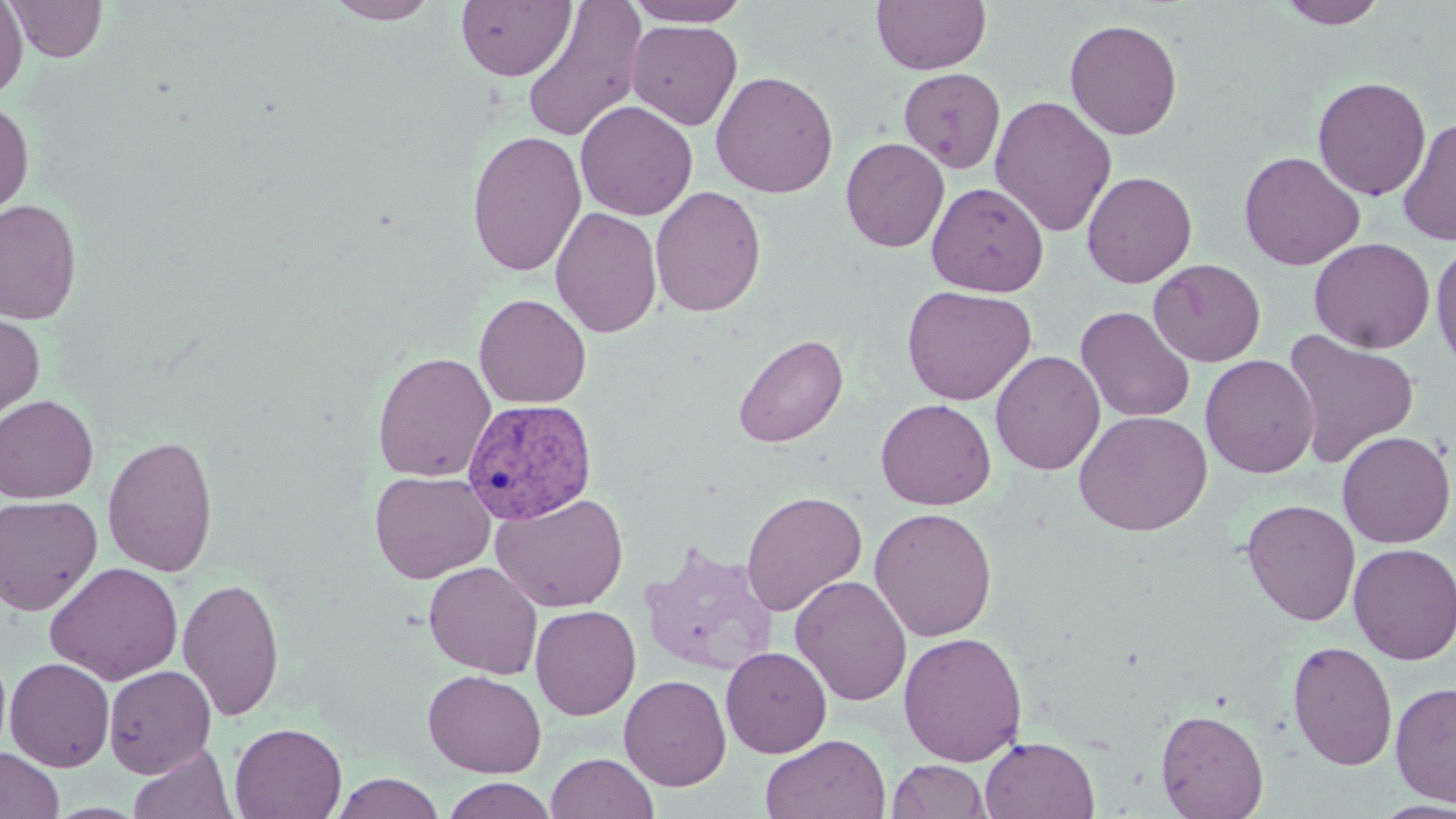

slide-level diagnosis = Plasmodium vivax
magnification = 1000x
preparation = thin blood film
stain = May-Grünwald-Giemsa
image size = 1456×819 pixels
modality = light microscopy
Plasmodium vivax-infected red blood cell locations = approximate bounding boxes as [x1, y1, x2, y2] in pixels: [461, 398, 597, 524]
uninfected red blood cell locations = approximate bounding boxes as [x1, y1, x2, y2] in pixels: [0, 0, 28, 100], [8, 0, 106, 63], [325, 0, 441, 24], [455, 0, 575, 81], [521, 0, 647, 144], [625, 0, 751, 27], [871, 0, 991, 74], [1276, 0, 1388, 29], [627, 19, 743, 130], [1064, 19, 1183, 140], [898, 67, 1006, 174], [711, 70, 839, 198], [1312, 76, 1431, 201], [990, 95, 1117, 237], [0, 100, 34, 218], [575, 100, 697, 221], [1397, 117, 1456, 247], [467, 130, 587, 277], [840, 136, 950, 253], [1239, 151, 1365, 270], [1082, 170, 1198, 288], [927, 181, 1049, 297], [650, 185, 766, 317], [0, 198, 82, 325], [550, 206, 662, 338], [1309, 237, 1435, 354], [1431, 240, 1456, 375], [1148, 259, 1266, 366], [901, 284, 1038, 406], [474, 293, 591, 409], [1076, 305, 1196, 422], [0, 311, 45, 428], [1282, 329, 1420, 468], [732, 333, 849, 448], [990, 350, 1105, 475], [372, 351, 496, 483], [1200, 354, 1320, 478], [0, 394, 99, 502], [876, 398, 996, 510], [1074, 410, 1213, 536], [1337, 430, 1455, 548], [102, 434, 219, 578], [370, 470, 495, 583], [741, 490, 867, 617], [491, 492, 628, 612], [0, 495, 103, 615], [1241, 499, 1361, 627], [869, 506, 998, 642], [639, 542, 780, 677], [1349, 542, 1456, 665], [424, 561, 543, 679], [45, 562, 183, 684], [790, 575, 912, 706], [177, 576, 286, 722], [530, 605, 641, 720], [898, 631, 1027, 766], [1287, 639, 1398, 771], [721, 646, 832, 757], [0, 647, 12, 761], [4, 657, 115, 772], [103, 664, 217, 778], [423, 669, 547, 778], [619, 674, 731, 792], [1390, 680, 1456, 808], [1156, 708, 1269, 819], [229, 722, 347, 819], [761, 734, 891, 819], [980, 735, 1100, 819], [128, 743, 237, 819], [0, 747, 64, 819], [546, 752, 658, 819], [887, 759, 991, 818], [330, 772, 446, 818], [442, 777, 558, 819], [1371, 800, 1456, 818]
field of view = single